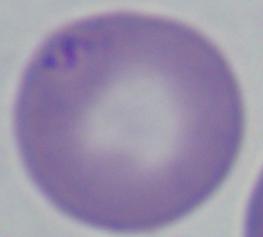
magnification = 1000x
identification = Babesia
modality = micrograph